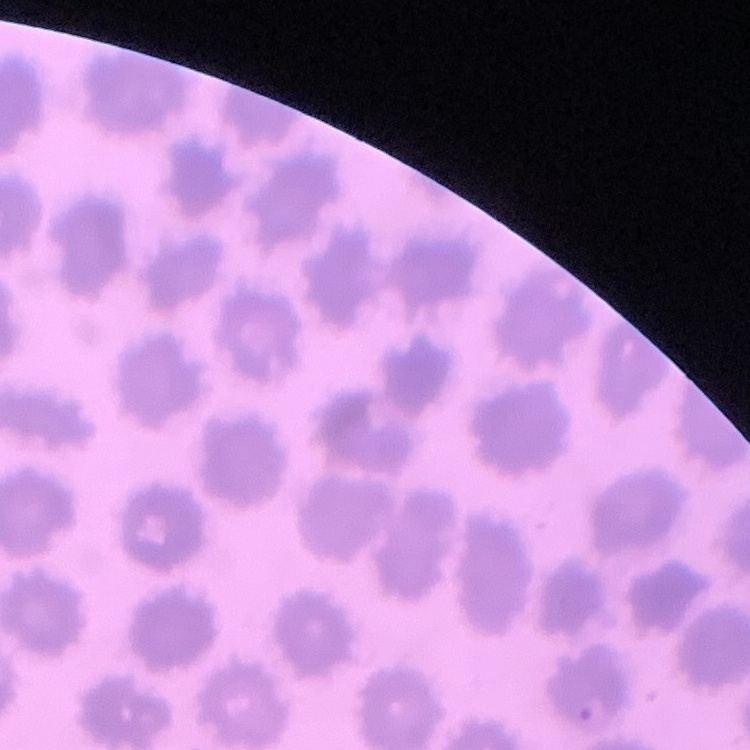
{
  "erythrocyte_morphology": "no rouleaux formation",
  "image_type": "one tile cut from a larger photomicrograph",
  "preparation": "thin blood smear",
  "stain": "Field's or Giemsa"
}